Identify the cell.
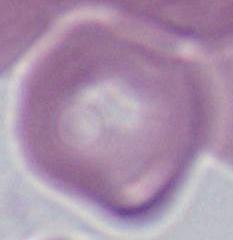

This is an erythrocyte.

Photomicrograph. 1000x magnification.